Name the parasite shown.
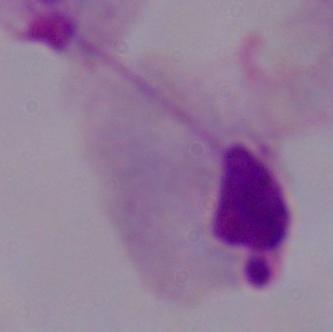
A trichomonad.

Summary:
  - Magnification: 1000x
  - Modality: micrograph